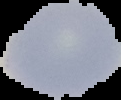 Result: negative for malaria parasites. From a thin blood film. Cell region segmented out of the field of view; the surrounding area is masked to black. Image is 121×100 pixels.